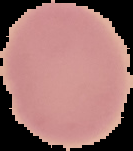
Summary:
  - Image size: 133×151 pixels
  - Result: no malaria parasites detected
  - Preparation: thin blood smear
  - Image type: segmented cell region with the area outside set to black